Comment on the morphology of the red blood cells.
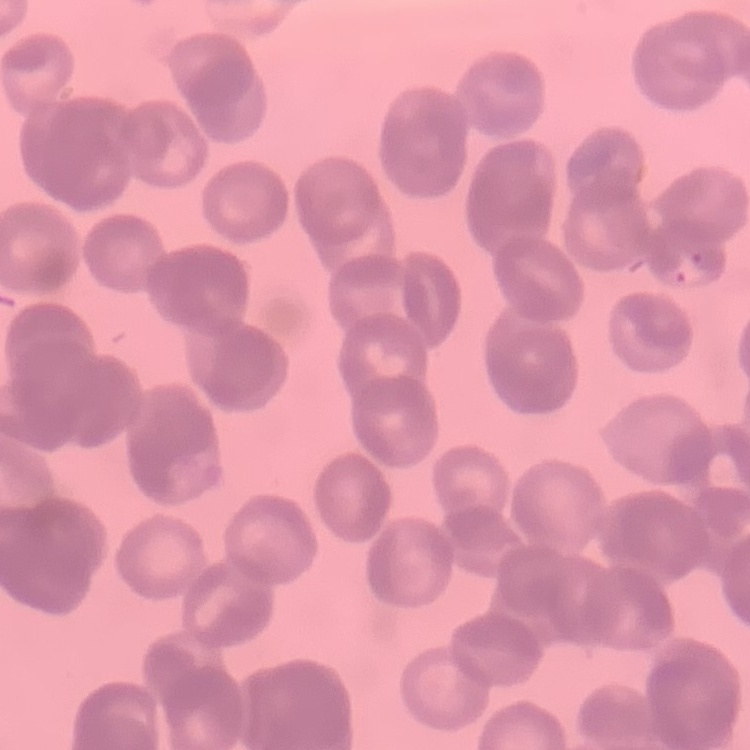

They show rouleaux formation.

Field's or Giemsa stain. One tile cut from a larger photomicrograph. Thin blood film.